Assess the morphology of the red blood cells.
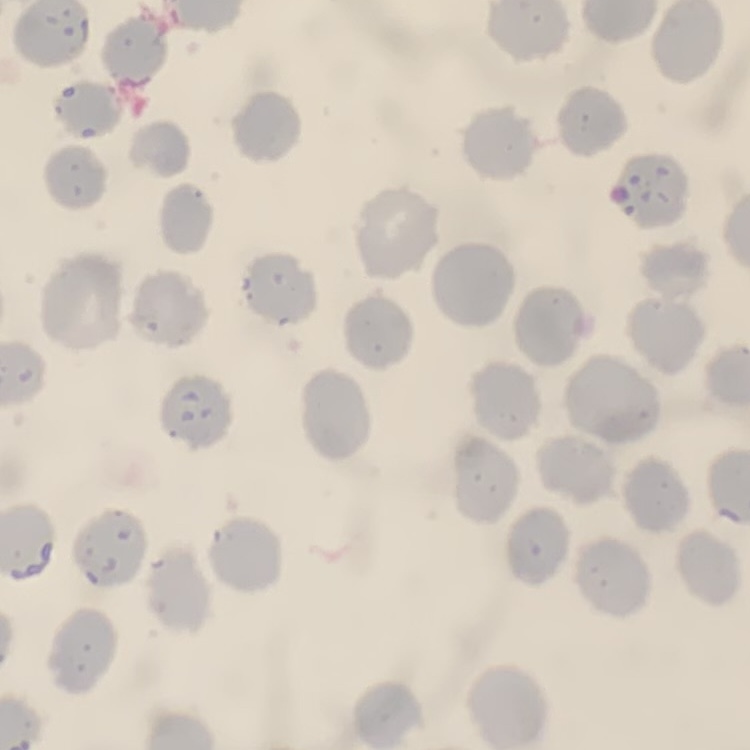
No rouleaux formation.

preparation = thin blood smear
stain = Field's or Giemsa
image type = one tile cut from a larger photomicrograph